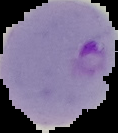

image type = segmented cell region with the area outside set to black
image size = 118×133 pixels
preparation = thin blood smear
result = malaria parasites identified